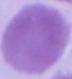
Summary:
  - Modality: photomicrograph
  - Identification: red blood cell
  - Magnification: 1000x